Give the position of every leukocyte visible.
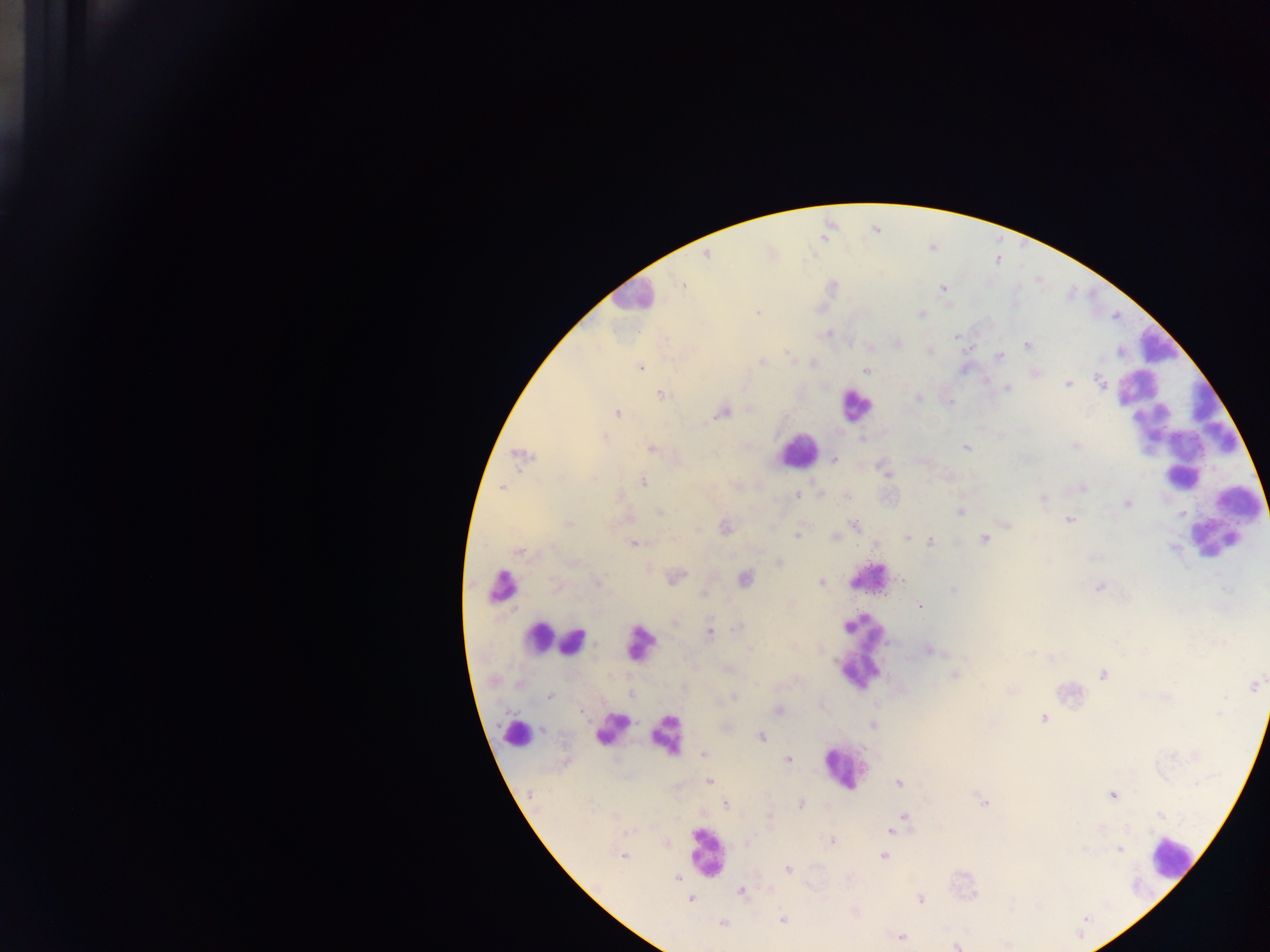

Approximate centers as {x, y} in pixels.
Leukocytes: {632, 296}, {1156, 344}, {854, 405}, {1181, 435}, {797, 450}, {1242, 504}, {1213, 540}, {866, 578}, {497, 584}, {538, 636}, {639, 642}, {572, 643}, {860, 649}, {610, 725}, {513, 733}, {666, 736}, {843, 767}, {706, 853}, {1171, 858}.

Summary:
  - Plasmodium parasite locations: {706, 255}, {684, 286}, {943, 288}, {758, 313}, {921, 314}, {827, 333}, {956, 335}, {898, 343}, {1028, 345}, {870, 347}, {930, 351}, {1000, 356}, {762, 362}, {640, 367}, {866, 370}, {1036, 373}, {1099, 381}, {1067, 384}, {1007, 388}, {661, 395}, {918, 398}, {950, 402}, {618, 413}, {723, 413}, {605, 438}, {861, 439}, {1075, 446}, {965, 448}, {651, 449}, {520, 455}, {834, 459}, {884, 470}, {593, 478}, {642, 481}, {502, 488}, {1082, 488}, {797, 495}, {1042, 499}, {1127, 504}, {960, 511}, {660, 513}, {1069, 520}, {568, 524}, {854, 524}, {726, 528}, {798, 537}, {836, 537}, {907, 537}, {984, 538}, {930, 541}, {632, 543}, {1173, 548}, {519, 553}, {779, 562}, {676, 577}, {744, 578}, {903, 581}, {597, 582}, {821, 583}, {554, 585}, {1098, 587}, {1227, 589}, {953, 590}, {703, 594}, {921, 606}, {738, 627}, {710, 633}, {749, 649}, {929, 650}, {1051, 658}, {1103, 674}, {955, 675}, {520, 684}, {982, 685}, {1254, 686}, {1011, 691}, {630, 695}, {549, 696}, {734, 697}, {778, 710}, {1219, 713}, {1043, 718}, {873, 725}, {543, 729}, {761, 736}, {703, 754}, {787, 760}, {710, 781}, {899, 783}, {1196, 784}, {1112, 795}, {984, 802}, {726, 804}, {801, 804}, {1161, 815}, {769, 816}, {904, 816}, {900, 821}, {1101, 829}, {891, 832}, {832, 841}, {1119, 849}, {884, 856}, {622, 857}, {788, 869}, {677, 878}, {741, 891}, {921, 898}, {690, 899}, {782, 920}, {723, 923}, {901, 937}, {957, 946}
  - Preparation: thick blood film
  - Field of view: single
  - Capture: mobile-phone photograph through a microscope
  - Image size: 1270×952 pixels
  - Country: Ghana